Report the malaria status of this cell.
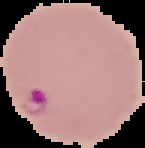

Parasitized.

image type = segmented cell region on a black background
preparation = thin blood film
image size = 145×148 pixels